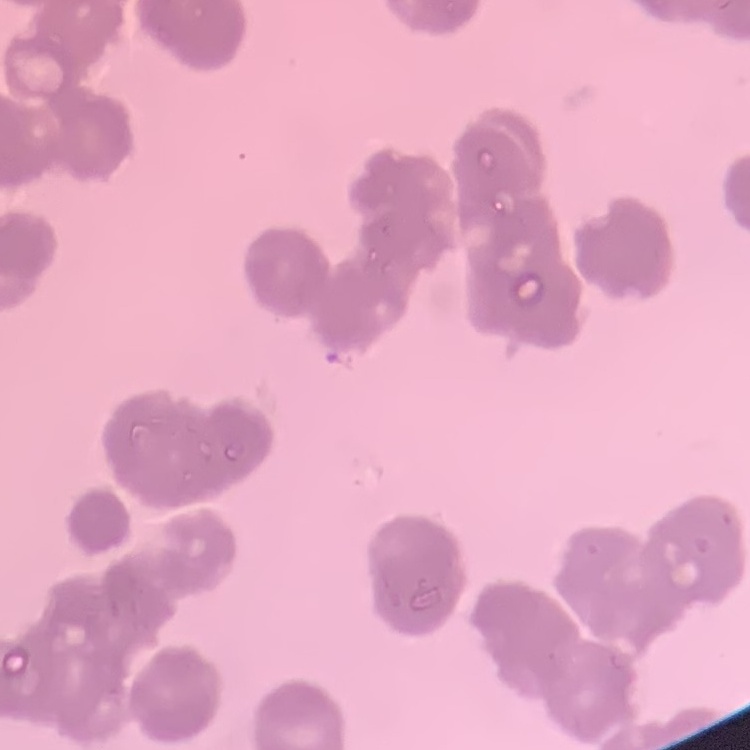
{
  "erythrocyte_morphology": "rouleaux formation",
  "image_type": "square crop of a larger photomicrograph",
  "preparation": "thin blood smear",
  "stain": "Field's or Giemsa"
}